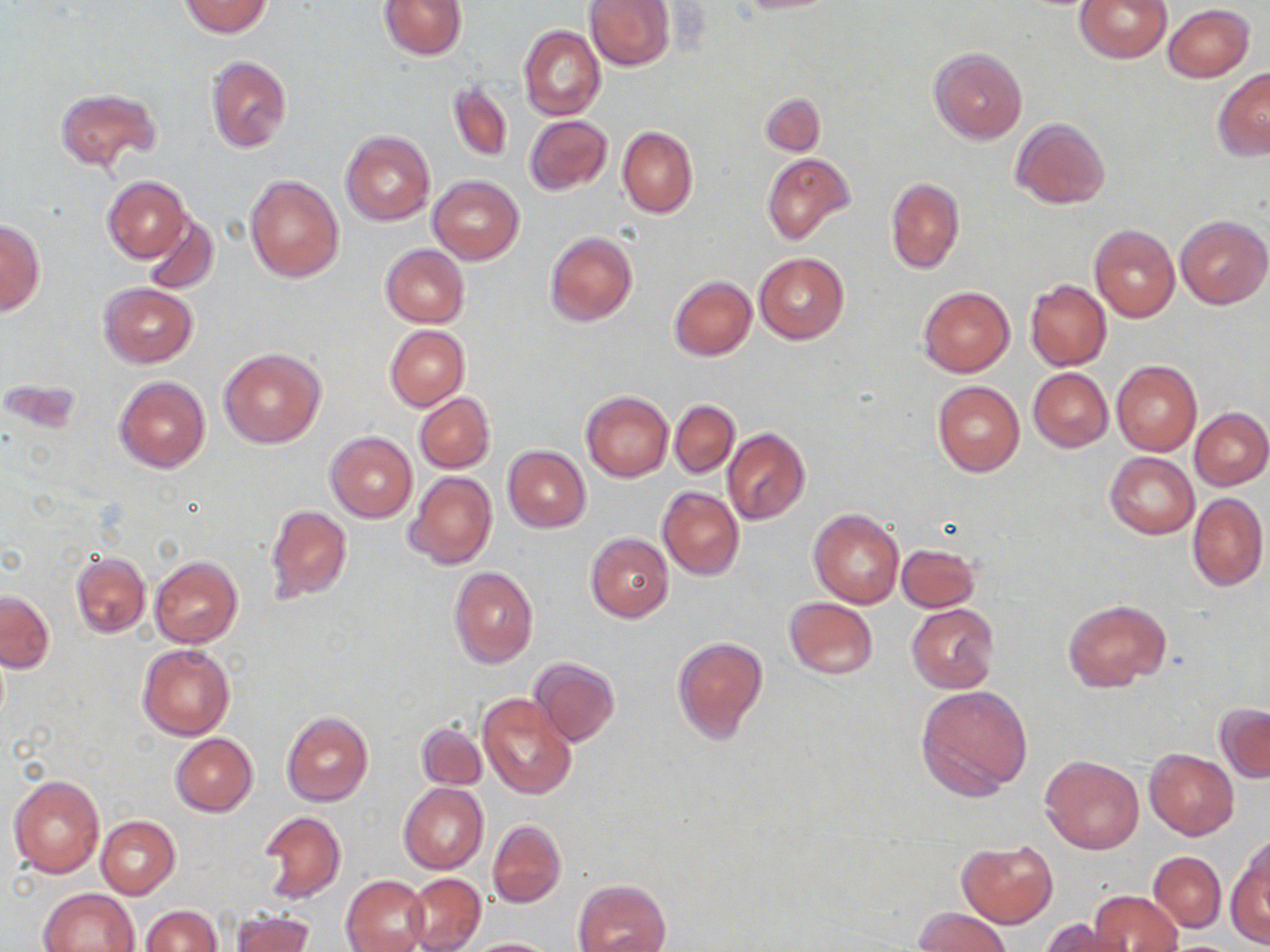
Summary:
  - Coordinate format: approximate bounding boxes as (x1, y1, x2, y2) in pixels
  - Uninfected red blood cell locations: (378, 0, 467, 59), (585, 0, 674, 70), (732, 0, 842, 14), (1075, 0, 1172, 63), (179, 1, 272, 37), (1163, 4, 1253, 82), (519, 25, 605, 121), (929, 47, 1028, 144), (205, 55, 293, 154), (1213, 68, 1270, 160), (448, 81, 513, 162), (54, 87, 161, 171), (761, 94, 824, 156), (523, 116, 611, 195), (1010, 118, 1110, 209), (617, 125, 698, 218), (341, 131, 434, 226), (762, 152, 855, 245), (243, 173, 345, 282), (428, 175, 524, 264), (103, 177, 191, 262), (885, 178, 964, 273), (141, 212, 218, 294), (1175, 214, 1270, 309), (1, 218, 45, 316), (1089, 225, 1180, 323), (545, 231, 638, 328), (381, 244, 469, 326), (754, 253, 849, 344), (669, 275, 757, 360), (1025, 280, 1111, 370), (99, 282, 197, 368), (918, 286, 1015, 376), (384, 325, 469, 411), (219, 348, 325, 448), (1111, 361, 1202, 455), (1028, 367, 1113, 452), (115, 375, 210, 473), (933, 381, 1025, 477), (581, 391, 674, 482), (414, 394, 494, 473), (669, 400, 740, 477), (1189, 408, 1270, 490), (722, 429, 810, 525), (326, 432, 417, 524), (503, 446, 590, 532), (1106, 453, 1199, 538), (406, 471, 497, 569), (658, 487, 744, 580), (1188, 492, 1267, 591), (266, 505, 352, 603), (810, 510, 904, 608), (585, 533, 674, 622), (897, 543, 979, 611), (71, 551, 151, 639), (150, 556, 242, 648), (449, 566, 538, 668), (1, 591, 53, 672), (784, 597, 877, 680), (1064, 598, 1171, 692), (907, 604, 999, 692), (672, 635, 768, 743), (137, 645, 235, 740), (530, 657, 620, 746), (916, 684, 1033, 799), (478, 693, 577, 799), (1216, 703, 1270, 783), (281, 711, 374, 806), (416, 720, 487, 790), (169, 733, 257, 816), (1144, 749, 1238, 838), (1039, 754, 1143, 854), (9, 774, 105, 880), (398, 783, 488, 874), (259, 811, 345, 902), (94, 815, 180, 898), (488, 818, 566, 907), (956, 841, 1057, 927), (1228, 845, 1270, 946), (1149, 851, 1225, 931), (404, 873, 486, 951), (341, 874, 429, 952), (575, 879, 671, 952), (39, 888, 140, 952), (1089, 891, 1184, 952), (142, 907, 222, 952), (914, 907, 1010, 952), (232, 909, 314, 952), (1043, 919, 1125, 952), (463, 938, 560, 951)
  - Slide-level diagnosis: negative for blood parasites
  - Preparation: thin blood smear
  - Image size: 1270×952 pixels
  - Magnification: 1000x
  - Modality: optical microscopy
  - Stain: May-Grünwald-Giemsa
  - Field of view: one of a larger specimen